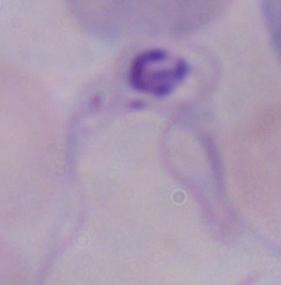
{
  "identification": "trypanosome",
  "magnification": "1000x",
  "modality": "photomicrograph"
}